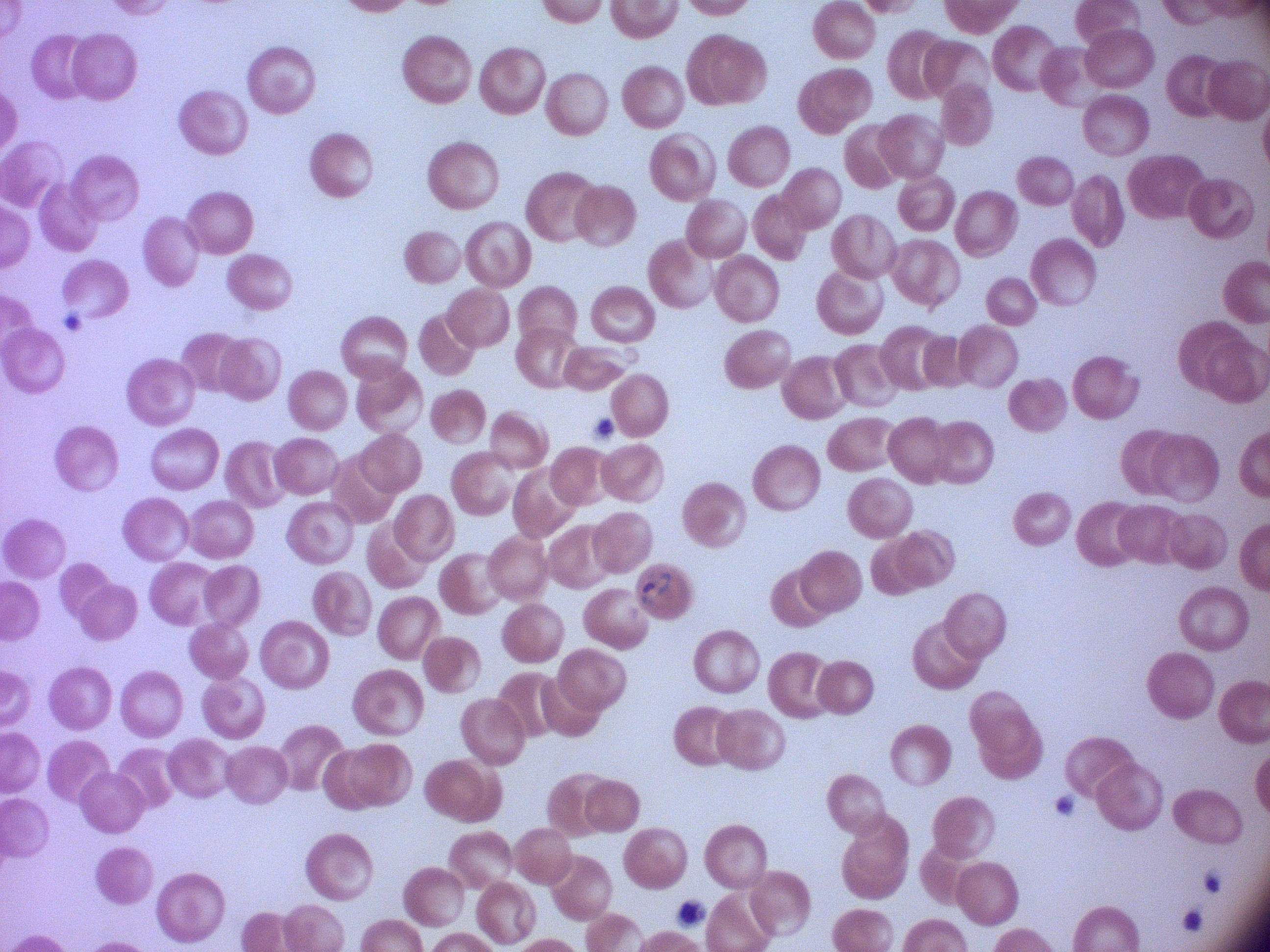
Approximate bounding boxes as (x1, y1, x2, y2) in pixels, from the source annotation, which is not necessarily exhaustive.
Summary:
  - Ring form locations: (632, 564, 679, 612)
  - Stain: Giemsa
  - Magnification: 100x
  - Species: Plasmodium falciparum
  - Preparation: thin blood smear
  - Microscope: Leica DM2000 with built-in camera
  - Image size: 1270×952 pixels
  - Field of view: one from this slide